Report the malaria status of this cell.
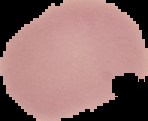

It is uninfected.

Summary:
  - Image size: 148×121 pixels
  - Image type: cell region segmented out of the field of view; surrounding area masked to black
  - Preparation: thin blood smear